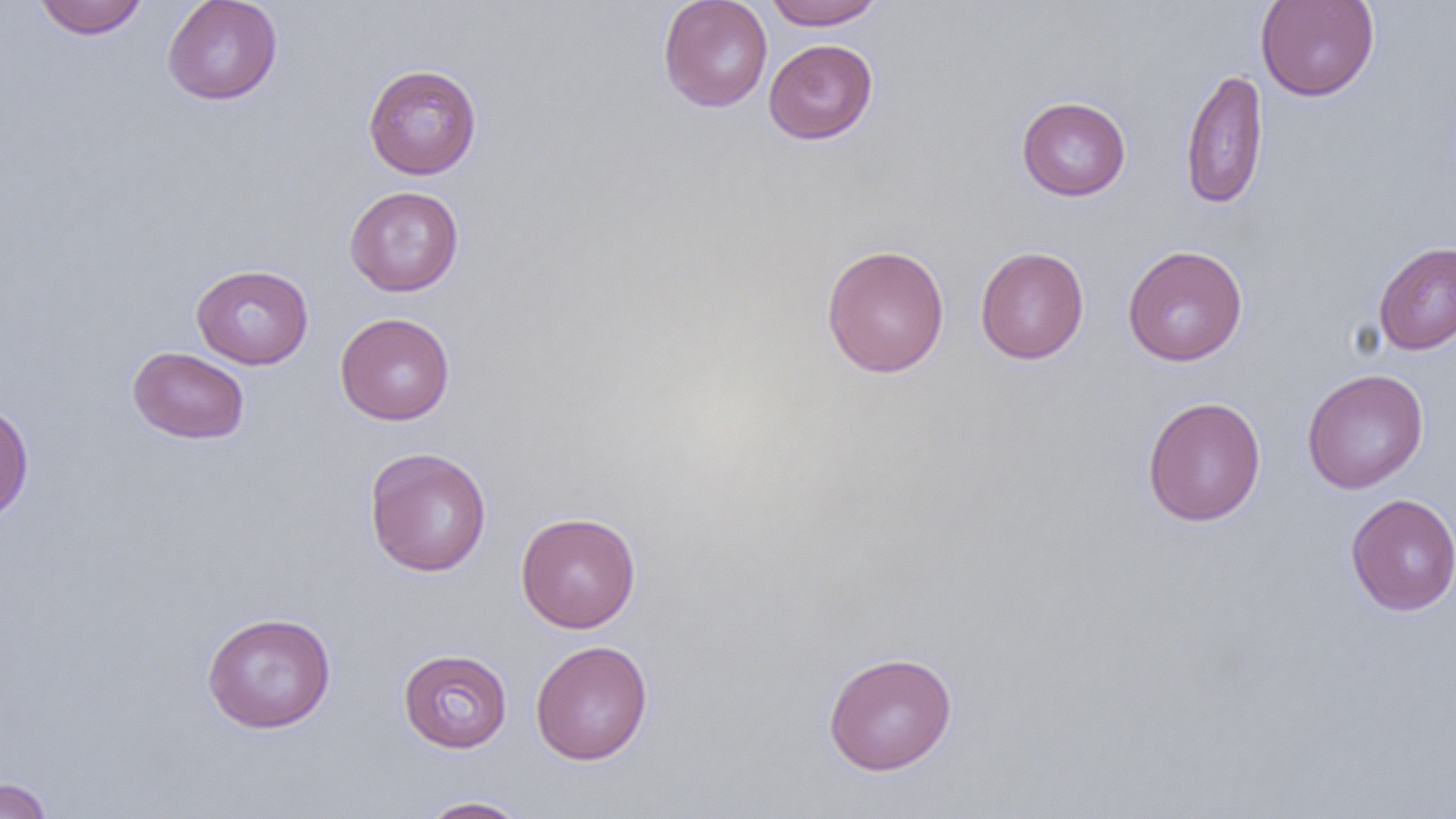
Summary:
  - Coordinate format: approximate bounding boxes as (x1, y1, x2, y2) in pixels
  - Uninfected red blood cell locations: (33, 0, 148, 39), (162, 0, 283, 105), (658, 0, 773, 112), (763, 0, 886, 30), (1254, 0, 1380, 101), (763, 39, 878, 144), (362, 63, 482, 180), (1180, 68, 1269, 210), (1016, 96, 1131, 201), (344, 185, 465, 296), (341, 187, 458, 424), (1373, 241, 1456, 355), (820, 244, 950, 378), (1122, 245, 1248, 366), (975, 246, 1089, 364), (191, 263, 313, 369), (335, 312, 455, 426), (127, 346, 250, 445), (1302, 368, 1429, 494), (1141, 396, 1266, 526), (0, 400, 34, 524), (364, 446, 492, 577), (1345, 493, 1456, 616), (515, 511, 641, 633), (201, 612, 337, 733), (530, 640, 653, 764), (397, 648, 513, 752), (822, 651, 958, 776), (0, 776, 55, 819), (417, 796, 531, 818)
  - Slide-level diagnosis: negative for blood parasites
  - Field of view: single
  - Image size: 1456×819 pixels
  - Preparation: thin blood film
  - Modality: optical microscopy
  - Magnification: 1000x